Locate every Plasmodium parasite.
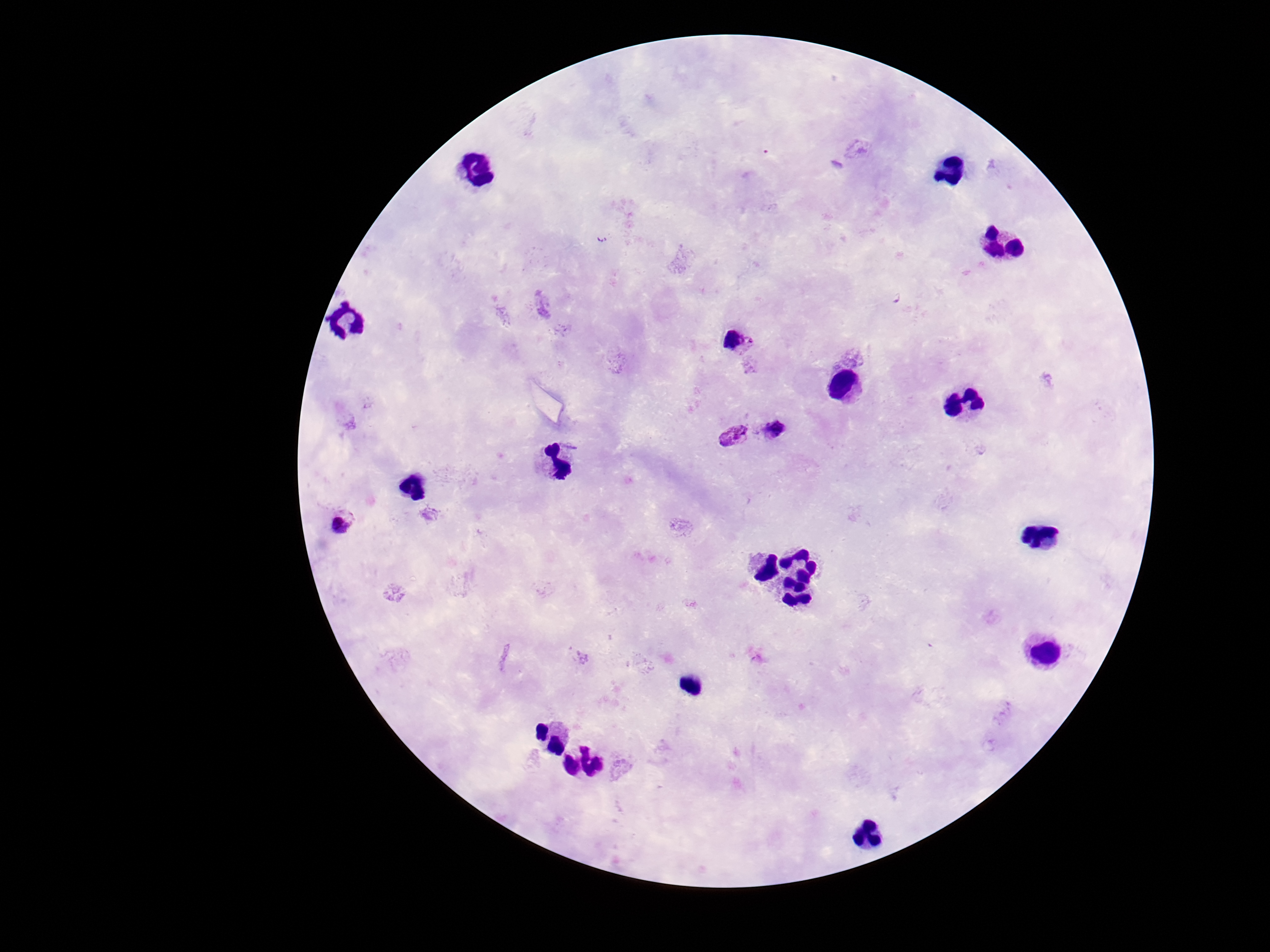

Approximate centers as (x, y) in pixels.
Plasmodium parasites: (601, 238), (895, 299), (736, 342), (776, 427), (733, 438), (341, 522).

Thick peripheral-blood smear. Giemsa stain. 100x magnification. Image is 1270×952 pixels. Patient malaria status: positive. Photographed through the microscope eyepiece with a smartphone camera. One field from this slide.